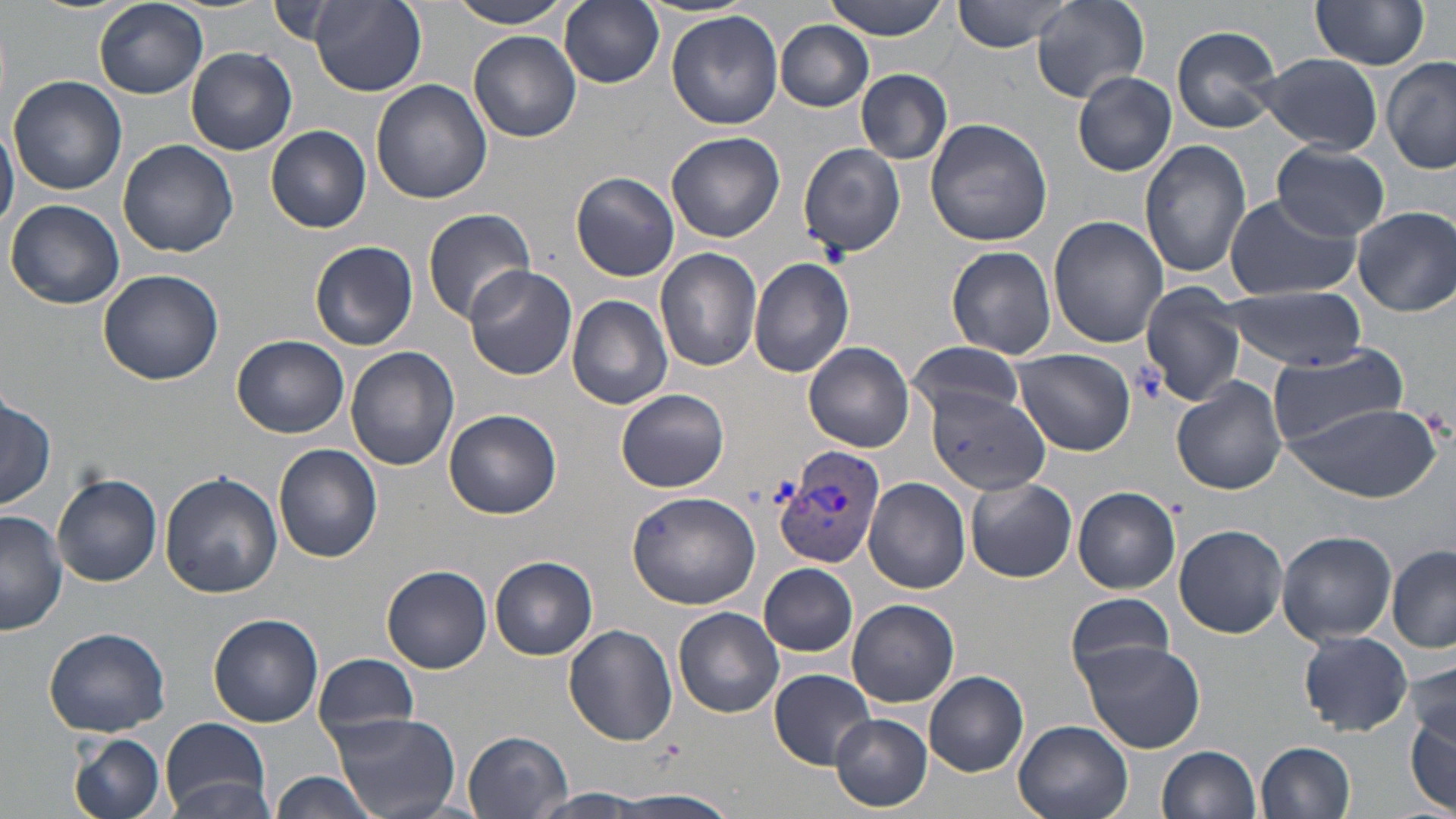

Approximate bounding boxes as named x1/y1/x2/y2 corners in pixels. Uninfected red blood cell locations: (x1=93, y1=0, x2=209, y2=99), (x1=447, y1=0, x2=576, y2=28), (x1=559, y1=0, x2=664, y2=89), (x1=825, y1=0, x2=951, y2=41), (x1=951, y1=0, x2=1077, y2=52), (x1=1028, y1=0, x2=1150, y2=103), (x1=1311, y1=0, x2=1431, y2=73), (x1=309, y1=2, x2=427, y2=96), (x1=264, y1=3, x2=358, y2=49), (x1=665, y1=10, x2=783, y2=130), (x1=775, y1=21, x2=874, y2=112), (x1=1171, y1=25, x2=1283, y2=134), (x1=468, y1=30, x2=582, y2=142), (x1=187, y1=48, x2=297, y2=155), (x1=1255, y1=53, x2=1383, y2=154), (x1=1382, y1=58, x2=1456, y2=176), (x1=856, y1=69, x2=952, y2=165), (x1=1073, y1=71, x2=1177, y2=177), (x1=7, y1=75, x2=128, y2=195), (x1=370, y1=79, x2=493, y2=205), (x1=0, y1=115, x2=18, y2=235), (x1=925, y1=117, x2=1053, y2=248), (x1=266, y1=125, x2=371, y2=234), (x1=666, y1=131, x2=785, y2=243), (x1=118, y1=139, x2=238, y2=258), (x1=1141, y1=139, x2=1251, y2=278), (x1=1270, y1=141, x2=1390, y2=239), (x1=798, y1=143, x2=905, y2=257), (x1=571, y1=172, x2=680, y2=282), (x1=1224, y1=193, x2=1361, y2=301), (x1=6, y1=199, x2=125, y2=310), (x1=1352, y1=207, x2=1456, y2=316), (x1=422, y1=208, x2=534, y2=324), (x1=1048, y1=215, x2=1168, y2=349), (x1=309, y1=241, x2=419, y2=351), (x1=947, y1=246, x2=1056, y2=358), (x1=654, y1=247, x2=762, y2=371), (x1=749, y1=256, x2=855, y2=377), (x1=463, y1=265, x2=578, y2=380), (x1=97, y1=268, x2=221, y2=387), (x1=1137, y1=284, x2=1246, y2=406), (x1=1222, y1=286, x2=1368, y2=368), (x1=567, y1=293, x2=673, y2=409), (x1=232, y1=334, x2=349, y2=438), (x1=904, y1=339, x2=1028, y2=421), (x1=804, y1=342, x2=915, y2=452), (x1=1266, y1=345, x2=1412, y2=446), (x1=345, y1=347, x2=459, y2=471), (x1=1012, y1=349, x2=1136, y2=456), (x1=1173, y1=376, x2=1287, y2=495), (x1=616, y1=388, x2=730, y2=493), (x1=928, y1=390, x2=1052, y2=495), (x1=0, y1=396, x2=55, y2=511), (x1=1285, y1=400, x2=1440, y2=501), (x1=445, y1=409, x2=562, y2=519), (x1=274, y1=444, x2=384, y2=563), (x1=160, y1=470, x2=282, y2=597), (x1=52, y1=474, x2=162, y2=587), (x1=864, y1=477, x2=970, y2=594), (x1=966, y1=477, x2=1077, y2=583), (x1=1074, y1=486, x2=1181, y2=594), (x1=627, y1=491, x2=761, y2=609), (x1=0, y1=511, x2=66, y2=634), (x1=1174, y1=524, x2=1287, y2=638), (x1=1277, y1=531, x2=1397, y2=643), (x1=1387, y1=548, x2=1456, y2=652), (x1=491, y1=556, x2=599, y2=660), (x1=759, y1=563, x2=859, y2=658), (x1=381, y1=566, x2=493, y2=674), (x1=1066, y1=593, x2=1178, y2=683), (x1=847, y1=599, x2=958, y2=707), (x1=673, y1=607, x2=784, y2=718), (x1=209, y1=614, x2=323, y2=726), (x1=564, y1=625, x2=679, y2=745), (x1=45, y1=627, x2=170, y2=736), (x1=1298, y1=631, x2=1412, y2=736), (x1=1075, y1=640, x2=1204, y2=753), (x1=314, y1=654, x2=420, y2=743), (x1=1407, y1=660, x2=1455, y2=752), (x1=768, y1=669, x2=876, y2=768), (x1=924, y1=672, x2=1028, y2=777), (x1=1405, y1=702, x2=1454, y2=814), (x1=330, y1=712, x2=460, y2=818), (x1=830, y1=713, x2=933, y2=812), (x1=159, y1=717, x2=271, y2=815), (x1=1014, y1=721, x2=1133, y2=819), (x1=463, y1=731, x2=571, y2=818), (x1=69, y1=733, x2=166, y2=819), (x1=1257, y1=740, x2=1357, y2=819), (x1=1156, y1=745, x2=1261, y2=819), (x1=271, y1=773, x2=376, y2=819), (x1=168, y1=778, x2=279, y2=818), (x1=529, y1=790, x2=649, y2=817), (x1=615, y1=791, x2=735, y2=819). Plasmodium vivax-infected red blood cell locations: (x1=773, y1=445, x2=886, y2=573). Slide-level diagnosis: Plasmodium vivax. Captured at 1000x magnification. Image is 1456×819 pixels. Single field of view. Optical microscopy. May-Grünwald-Giemsa stain. Thin blood smear.